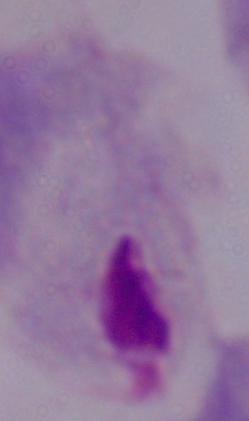

Summary:
  - Identification: trichomonad
  - Modality: micrograph
  - Magnification: 1000x